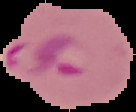

image_type: segmented cell region with the area outside set to black
malaria_status: parasitized
preparation: thin blood film
image_size: 136×112 pixels